Name the blood parasite species.
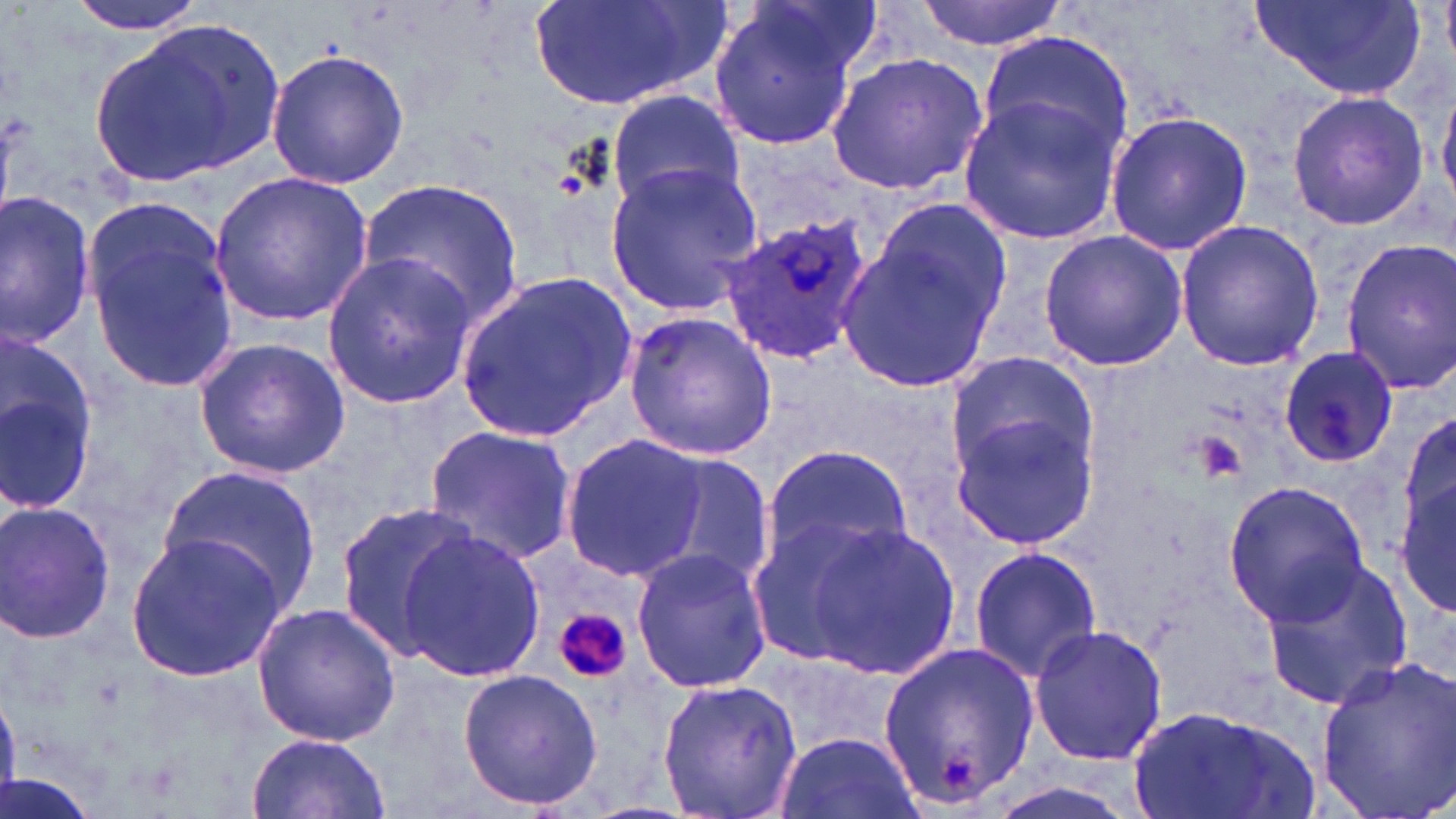

Plasmodium ovale.

Summary:
  - Coordinate format: approximate bounding boxes as named x1/y1/x2/y2 corners in pixels
  - Uninfected red blood cell locations: (x1=63, y1=0, x2=209, y2=36), (x1=525, y1=0, x2=731, y2=112), (x1=913, y1=0, x2=1075, y2=51), (x1=1246, y1=0, x2=1425, y2=103), (x1=1440, y1=0, x2=1455, y2=64), (x1=708, y1=3, x2=863, y2=148), (x1=90, y1=17, x2=291, y2=186), (x1=976, y1=27, x2=1139, y2=166), (x1=265, y1=49, x2=410, y2=190), (x1=826, y1=51, x2=992, y2=196), (x1=1437, y1=77, x2=1456, y2=211), (x1=606, y1=87, x2=744, y2=213), (x1=1285, y1=89, x2=1431, y2=232), (x1=959, y1=94, x2=1126, y2=243), (x1=1104, y1=108, x2=1253, y2=258), (x1=605, y1=163, x2=764, y2=315), (x1=210, y1=170, x2=373, y2=328), (x1=361, y1=178, x2=525, y2=328), (x1=0, y1=191, x2=97, y2=348), (x1=868, y1=197, x2=1012, y2=336), (x1=82, y1=199, x2=240, y2=387), (x1=1175, y1=219, x2=1326, y2=372), (x1=835, y1=226, x2=1003, y2=396), (x1=1038, y1=229, x2=1187, y2=372), (x1=1339, y1=239, x2=1456, y2=394), (x1=322, y1=252, x2=481, y2=412), (x1=455, y1=269, x2=635, y2=445), (x1=621, y1=310, x2=777, y2=461), (x1=0, y1=333, x2=100, y2=515), (x1=192, y1=337, x2=350, y2=478), (x1=1278, y1=346, x2=1397, y2=468), (x1=943, y1=350, x2=1099, y2=493), (x1=950, y1=413, x2=1098, y2=550), (x1=1400, y1=414, x2=1456, y2=542), (x1=423, y1=425, x2=579, y2=564), (x1=559, y1=437, x2=707, y2=582), (x1=764, y1=443, x2=914, y2=567), (x1=645, y1=450, x2=775, y2=594), (x1=157, y1=465, x2=321, y2=612), (x1=1396, y1=474, x2=1454, y2=618), (x1=1221, y1=480, x2=1371, y2=623), (x1=0, y1=500, x2=117, y2=645), (x1=336, y1=502, x2=481, y2=659), (x1=743, y1=510, x2=903, y2=671), (x1=799, y1=522, x2=958, y2=679), (x1=400, y1=528, x2=546, y2=685), (x1=123, y1=532, x2=288, y2=683), (x1=628, y1=544, x2=772, y2=695), (x1=966, y1=545, x2=1102, y2=683), (x1=1259, y1=556, x2=1415, y2=712), (x1=250, y1=601, x2=402, y2=747), (x1=1027, y1=625, x2=1169, y2=766), (x1=875, y1=637, x2=1041, y2=812), (x1=1314, y1=652, x2=1456, y2=819), (x1=457, y1=666, x2=601, y2=812), (x1=656, y1=676, x2=804, y2=819), (x1=1128, y1=701, x2=1317, y2=817), (x1=773, y1=730, x2=920, y2=819), (x1=245, y1=731, x2=389, y2=819), (x1=0, y1=774, x2=103, y2=819)
  - Platelet locations: (x1=551, y1=604, x2=633, y2=685)
  - Plasmodium ovale-infected red blood cell locations: (x1=721, y1=214, x2=870, y2=366)
  - Field of view: single
  - Magnification: 1000x
  - Preparation: thin blood film
  - Image size: 1456×819 pixels
  - Stain: May-Grünwald-Giemsa
  - Modality: light microscopy